State which parasite is depicted.
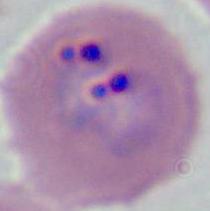
Plasmodium.

Photomicrograph. Captured at either 400x or 1000x magnification.